State which parasite is depicted.
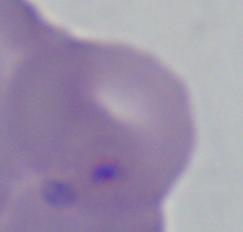
Babesia.

Captured at 1000x magnification. Micrograph.